Point out each malaria parasite and each leukocyte.
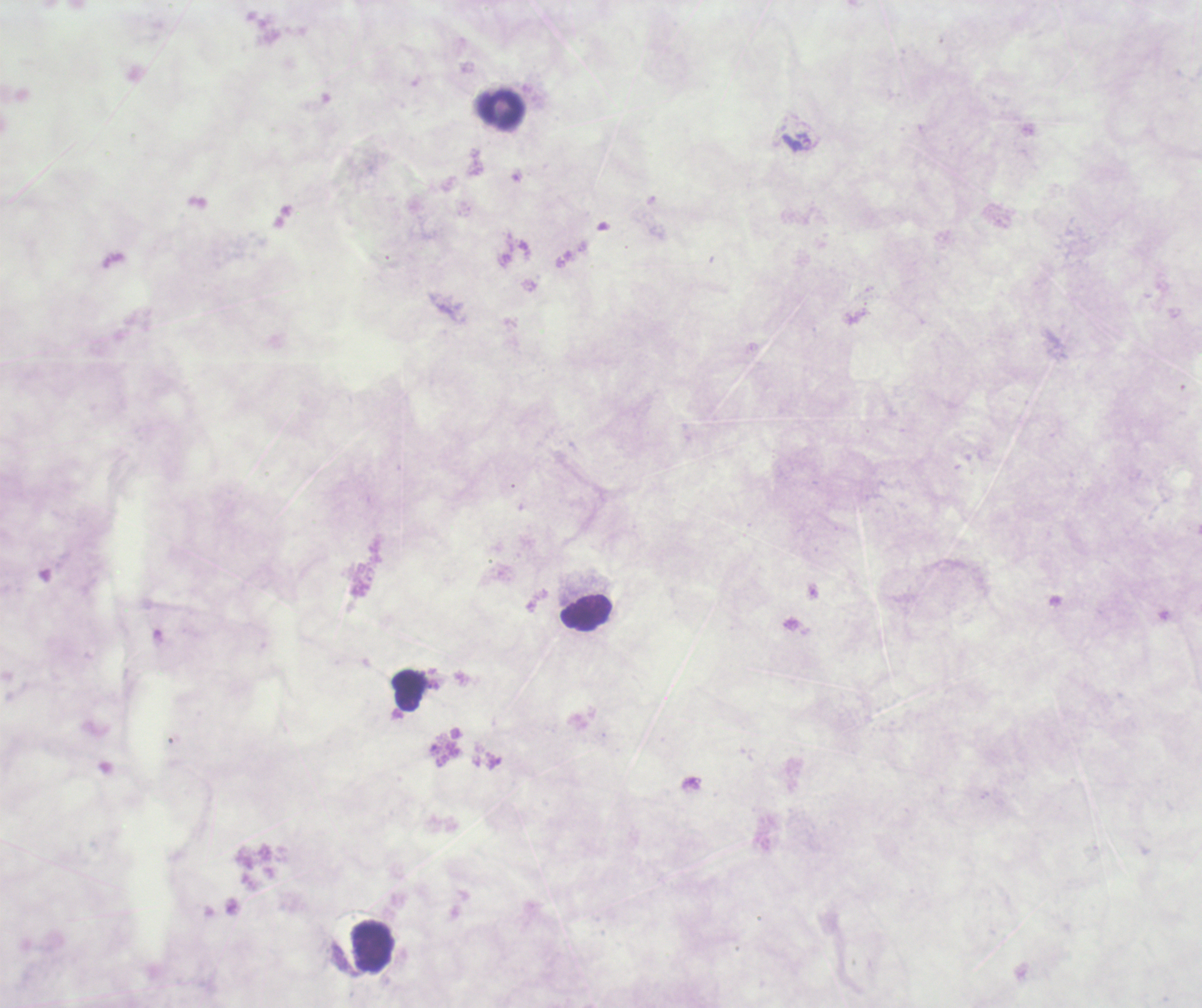

No malaria parasites detected.
Approximate centers as {x, y} in pixels.
Leukocytes: {500, 111}, {587, 612}, {410, 690}, {370, 949}.

stain = Romanowsky
field of view = single
context = previously used in a real diagnosis
background quality = poor
magnification = 100x
coloration quality = bad
preparation = thick blood film
image size = 1202×1008 pixels